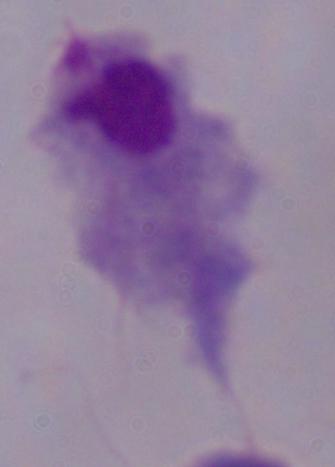 Photomicrograph. A trichomonad is shown. Captured at 1000x magnification.